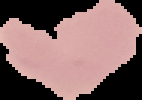

image size = 142×100 pixels
image type = segmented cell region with the area outside set to black
malaria status = uninfected
preparation = thin blood smear